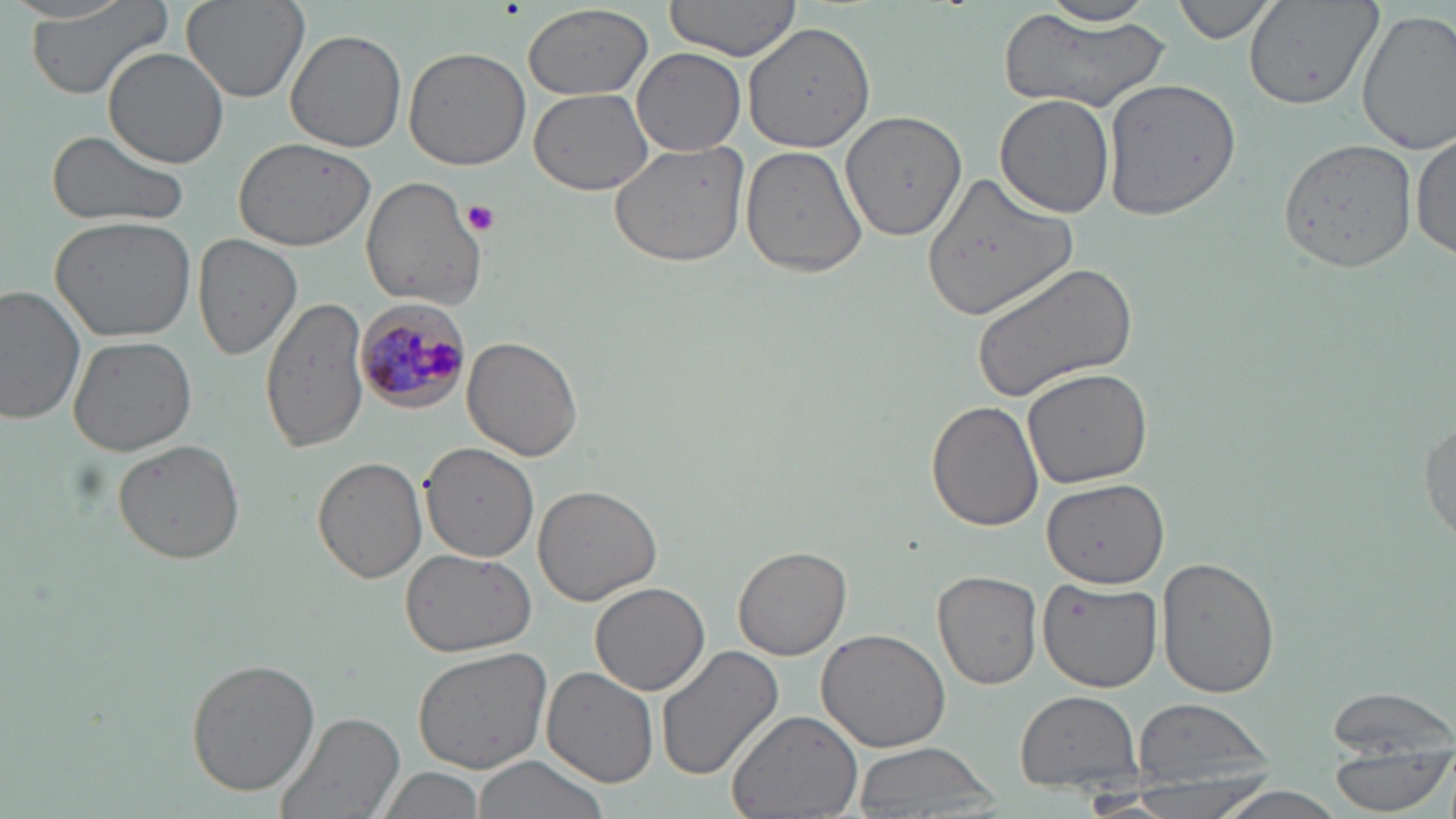 Approximate bounding boxes as (x1,y1)-(x2,y2) corner pairs in pixels. Plasmodium malariae-infected red blood cell locations: (355,298)-(470,412). Platelet locations: (462,198)-(501,235). Uninfected red blood cell locations: (21,0)-(176,103), (181,0)-(310,104), (662,0)-(804,60), (1173,0)-(1277,42), (1243,0)-(1379,110), (523,4)-(654,102), (1020,4)-(1166,29), (1001,10)-(1174,115), (1357,10)-(1456,153), (743,20)-(876,151), (287,29)-(408,153), (104,46)-(231,168), (402,46)-(532,173), (631,48)-(746,156), (1101,76)-(1245,221), (530,89)-(655,195), (991,94)-(1114,218), (840,108)-(967,243), (47,129)-(191,232), (1410,132)-(1455,261), (1277,137)-(1417,274), (232,138)-(376,251), (609,138)-(752,267), (740,145)-(868,279), (920,172)-(1075,324), (361,175)-(487,309), (49,213)-(196,341), (192,233)-(301,360), (971,262)-(1139,404), (1,285)-(87,425), (260,295)-(372,453), (68,336)-(198,457), (462,336)-(583,463), (1022,366)-(1152,488), (927,401)-(1046,532), (1419,409)-(1455,548), (111,439)-(246,566), (421,444)-(537,560), (313,456)-(427,584), (1041,477)-(1168,587), (532,484)-(661,605), (733,544)-(851,660), (398,546)-(535,658), (1157,557)-(1281,697), (933,569)-(1043,692), (1036,574)-(1163,694), (590,581)-(710,696), (815,628)-(951,754), (654,645)-(785,781), (412,646)-(552,773), (185,655)-(321,797), (542,666)-(660,789), (1325,683)-(1456,762), (1014,689)-(1145,797), (1129,698)-(1276,796), (725,708)-(864,819), (274,709)-(405,819), (853,743)-(1000,817), (1328,748)-(1450,816), (469,755)-(610,819), (376,763)-(485,819), (1203,785)-(1357,819). Slide-level diagnosis: Plasmodium malariae. May-Grünwald-Giemsa-stained preparation. Light microscopy. Single field of view. Captured at 1000x magnification. Image is 1456×819 pixels. Thin blood film.